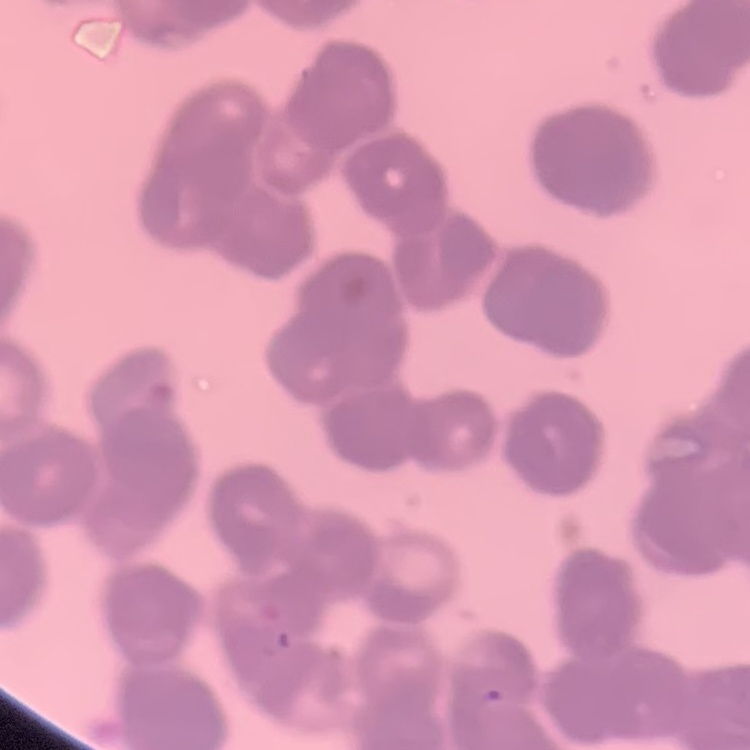

erythrocyte morphology = rouleaux formation
preparation = thin peripheral smear
image type = one tile cut from a larger photomicrograph
stain = Field's or Giemsa